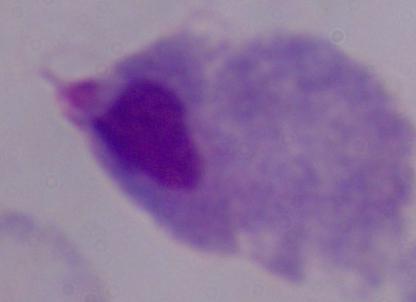

Captured at 1000x magnification. A trichomonad is shown. Photomicrograph.